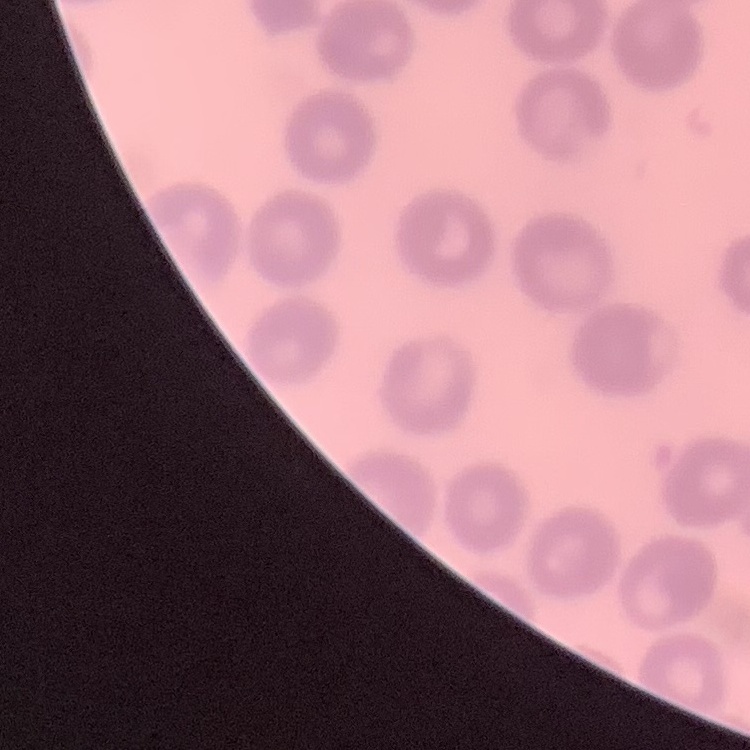

Summary:
  - Red blood cell morphology: no rouleaux formation
  - Image type: square crop of a larger photomicrograph
  - Stain: Field's or Giemsa
  - Preparation: thin blood film